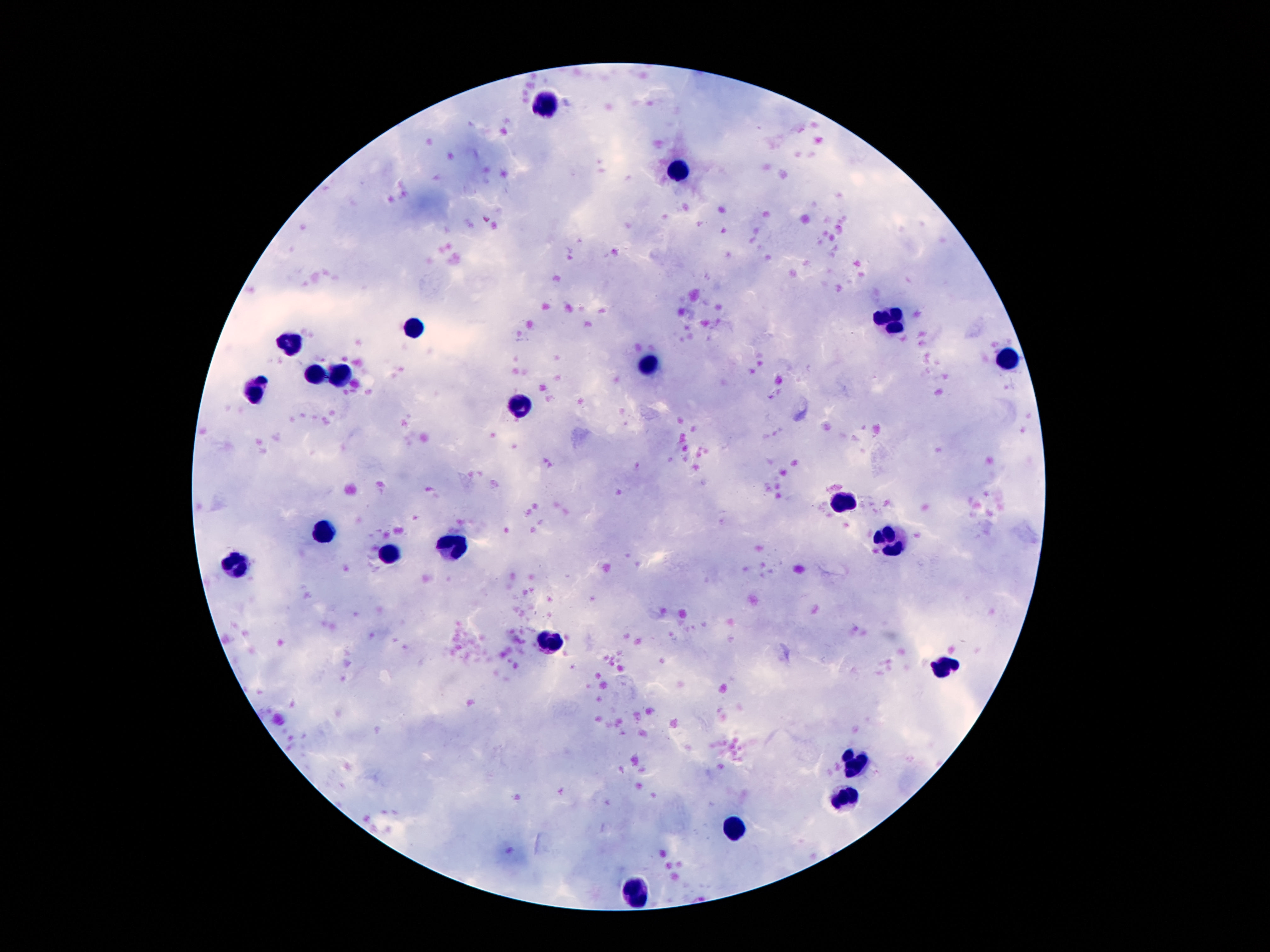

Approximate object centers, in pixels from the top-left corner.
Summary:
  - Leukocyte locations: (x=546, y=102), (x=681, y=172), (x=892, y=319), (x=413, y=325), (x=288, y=344), (x=1009, y=358), (x=647, y=365), (x=343, y=372), (x=315, y=374), (x=255, y=386), (x=518, y=409), (x=843, y=503), (x=321, y=532), (x=890, y=538), (x=452, y=546), (x=389, y=555), (x=237, y=564), (x=550, y=642), (x=944, y=665), (x=858, y=761), (x=845, y=799), (x=735, y=827), (x=638, y=892)
  - Stain: Giemsa
  - Field of view: single
  - Preparation: thick blood smear
  - Magnification: 100x
  - Patient malaria status: uninfected
  - Capture: smartphone camera through the microscope eyepiece
  - Image size: 1270×952 pixels